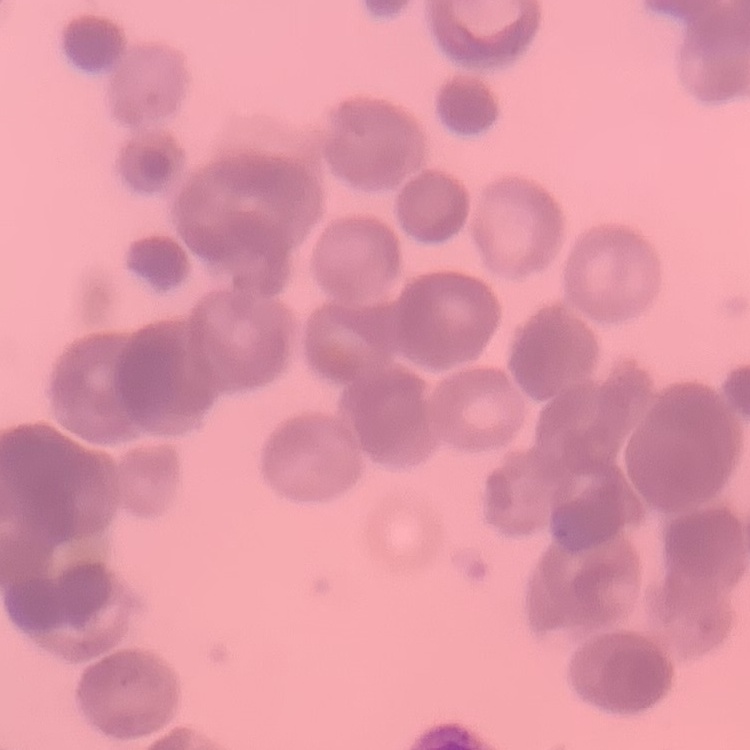

The erythrocytes show rouleaux formation. One tile cut from a larger photomicrograph. Thin blood smear. Stained with either Field's or Giemsa.